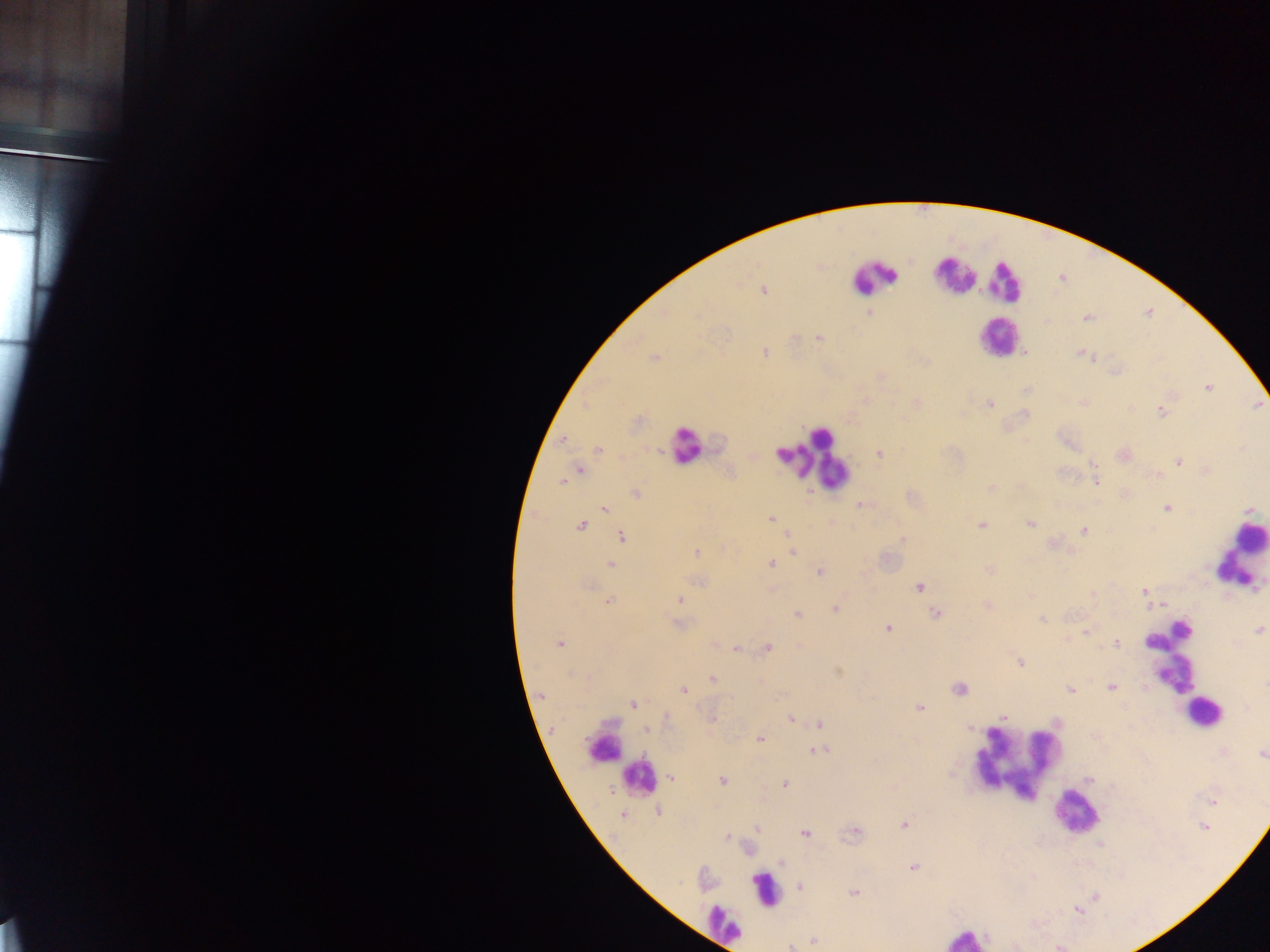

country = Ghana
leukocyte locations = approximate centers as {x, y} in pixels: {961, 274}, {874, 278}, {1006, 282}, {1001, 336}, {687, 446}, {830, 463}, {1241, 557}, {1170, 653}, {1206, 715}, {606, 747}, {1021, 760}, {640, 778}, {1074, 814}, {769, 892}, {716, 922}, {963, 939}
malaria parasite locations = approximate centers as {x, y} in pixels: {935, 274}, {764, 291}, {870, 314}, {819, 339}, {797, 341}, {766, 352}, {1088, 354}, {655, 358}, {1093, 358}, {1208, 388}, {990, 404}, {1162, 411}, {1026, 414}, {563, 439}, {598, 449}, {780, 453}, {879, 454}, {1179, 462}, {580, 470}, {805, 471}, {1207, 472}, {561, 481}, {990, 487}, {635, 494}, {861, 504}, {1167, 507}, {605, 510}, {770, 517}, {1029, 523}, {581, 524}, {980, 526}, {1083, 530}, {621, 536}, {900, 539}, {696, 551}, {792, 553}, {770, 563}, {611, 564}, {989, 569}, {820, 571}, {700, 581}, {919, 586}, {1145, 591}, {1093, 594}, {678, 598}, {610, 600}, {1164, 605}, {988, 606}, {835, 607}, {936, 613}, {797, 614}, {1042, 619}, {887, 628}, {1085, 631}, {1147, 643}, {560, 644}, {1116, 644}, {767, 647}, {735, 648}, {1019, 662}, {838, 672}, {710, 679}, {1110, 687}, {959, 689}, {1070, 689}, {684, 690}, {632, 704}, {918, 708}, {1002, 718}, {711, 719}, {790, 719}, {818, 724}, {645, 728}, {970, 728}, {760, 738}, {823, 749}, {813, 750}, {1262, 754}, {672, 777}, {670, 779}, {723, 781}, {784, 784}, {611, 792}, {657, 811}, {622, 815}, {904, 824}, {1201, 828}, {757, 829}, {805, 834}, {726, 837}, {781, 863}, {913, 867}, {799, 885}, {854, 894}, {813, 941}, {789, 947}
field of view = single
image size = 1270×952 pixels
preparation = thick blood film
capture = mobile-phone photograph through a microscope